Point out each Plasmodium parasite.
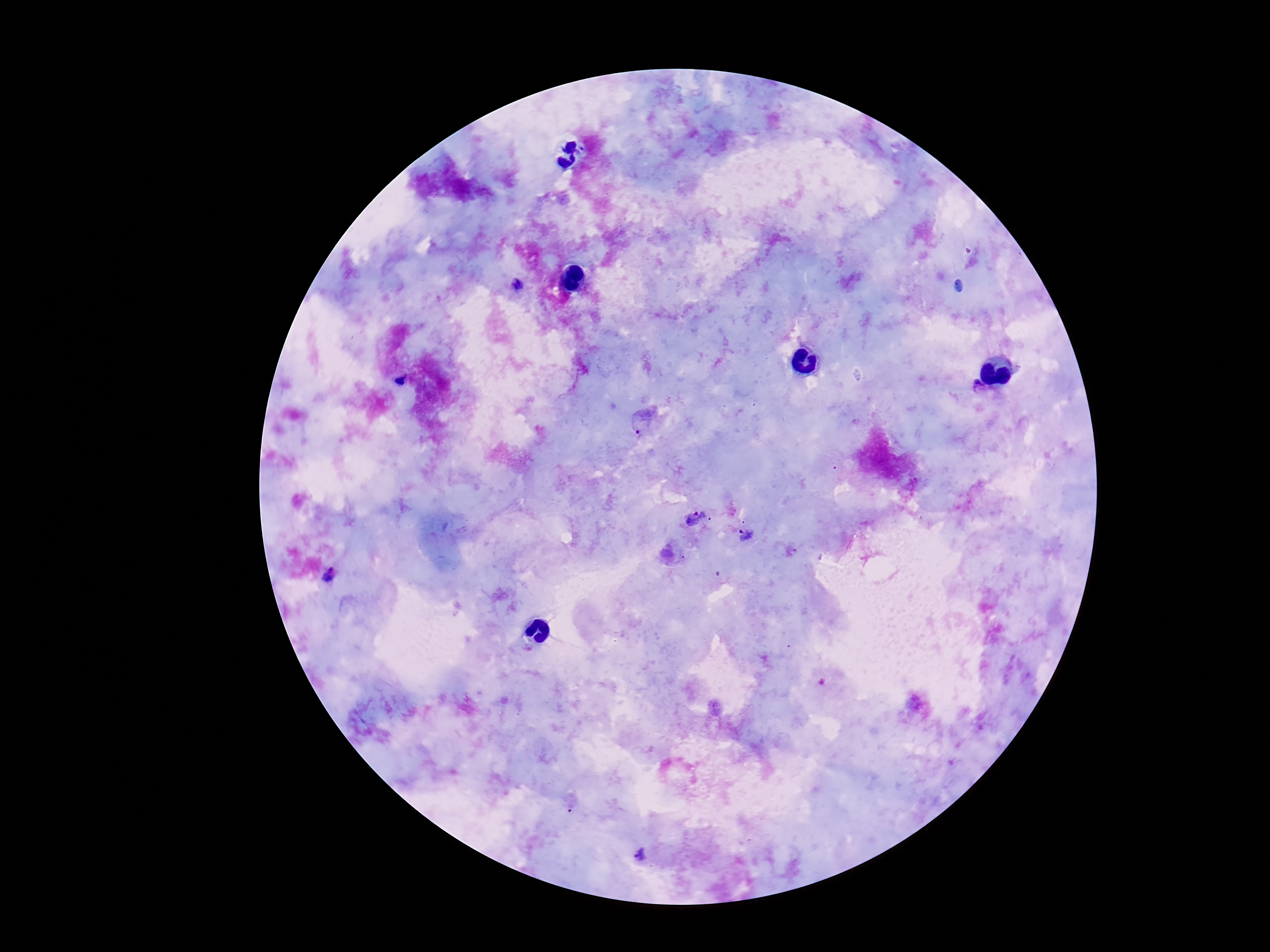
Approximate centers as [x, y] in pixels.
Plasmodium parasites: [518, 285], [644, 420], [696, 517], [744, 534], [329, 577], [642, 855].

preparation = thick peripheral-blood smear
image size = 1270×952 pixels
capture = smartphone camera through the microscope eyepiece
magnification = 100x
field of view = single
stain = Giemsa
patient malaria status = positive